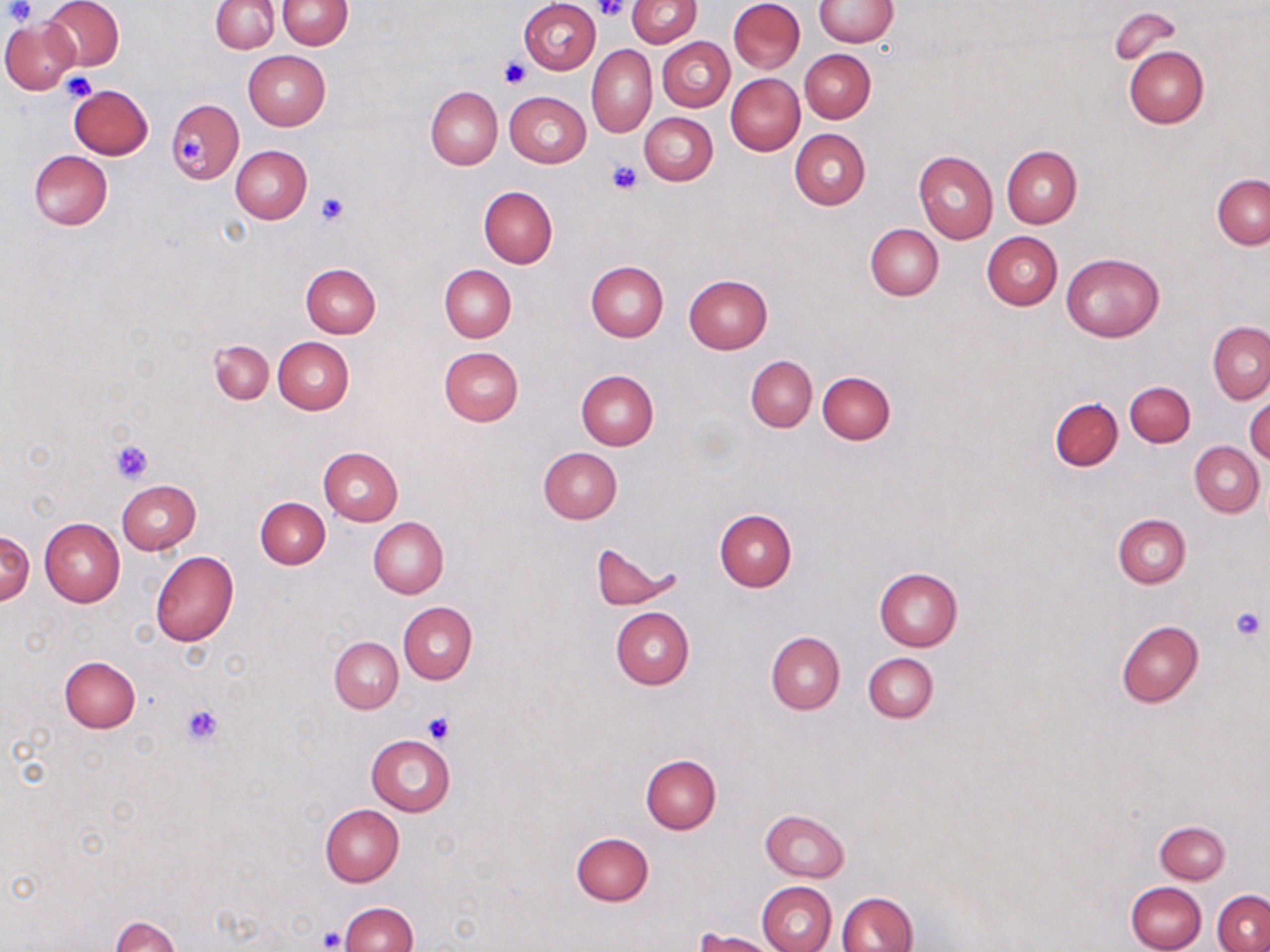 Approximate bounding boxes as (x1, y1, x2, y2) in pixels. Platelet locations: (3, 0, 35, 25), (597, 0, 629, 21), (499, 59, 529, 88), (61, 74, 96, 102), (177, 130, 208, 166), (606, 161, 641, 194), (315, 190, 351, 227), (110, 440, 153, 483), (1229, 607, 1268, 641), (180, 703, 223, 746), (426, 712, 454, 742), (318, 928, 345, 950). Uninfected red blood cell locations: (44, 0, 124, 71), (277, 0, 352, 49), (520, 0, 600, 73), (626, 0, 701, 47), (728, 0, 805, 73), (813, 0, 896, 47), (211, 1, 278, 53), (1111, 5, 1180, 63), (0, 17, 79, 94), (656, 37, 734, 112), (587, 45, 657, 137), (1123, 45, 1208, 129), (800, 49, 875, 122), (243, 51, 331, 130), (726, 73, 804, 155), (67, 83, 153, 159), (426, 86, 503, 169), (505, 91, 590, 168), (166, 98, 242, 185), (640, 112, 717, 185), (790, 129, 870, 209), (1001, 145, 1082, 227), (231, 146, 312, 223), (28, 149, 112, 230), (914, 149, 997, 243), (1211, 174, 1270, 249), (479, 185, 558, 268), (865, 223, 943, 301), (982, 231, 1062, 310), (1061, 252, 1165, 342), (586, 261, 668, 342), (301, 263, 381, 338), (440, 265, 516, 342), (682, 275, 771, 353), (1207, 321, 1270, 404), (273, 337, 354, 414), (210, 340, 273, 404), (438, 346, 523, 426), (746, 356, 817, 431), (575, 370, 658, 449), (817, 372, 894, 444), (1124, 381, 1195, 446), (1245, 394, 1270, 466), (1050, 395, 1123, 472), (1190, 442, 1264, 517), (318, 447, 403, 526), (538, 447, 622, 523), (117, 480, 201, 554), (255, 497, 329, 568), (714, 508, 797, 591), (1113, 513, 1191, 588), (368, 518, 448, 599), (41, 519, 125, 606), (0, 529, 34, 606), (590, 542, 676, 610), (150, 550, 239, 646), (873, 567, 962, 651), (399, 601, 477, 684), (611, 607, 694, 689), (1116, 620, 1203, 707), (766, 631, 844, 714), (330, 636, 403, 713), (863, 652, 938, 723), (59, 655, 140, 732), (365, 734, 455, 816), (641, 754, 721, 833), (320, 804, 403, 886), (760, 809, 849, 882), (1154, 820, 1230, 884), (572, 831, 653, 905), (757, 881, 836, 952), (1125, 881, 1206, 952), (1212, 889, 1269, 952), (836, 891, 917, 952), (339, 902, 417, 952), (112, 916, 181, 952), (695, 929, 778, 952). Slide-level diagnosis: negative for blood parasites. 1000x magnification. May-Grünwald-Giemsa stain. One field of a larger specimen. Optical microscopy. Thin blood smear. Image is 1270×952 pixels.